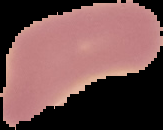
{
  "malaria_status": "uninfected",
  "image_size": "163×130 pixels",
  "preparation": "thin blood film",
  "image_type": "segmented cell region on a black background"
}